Locate every malaria parasite.
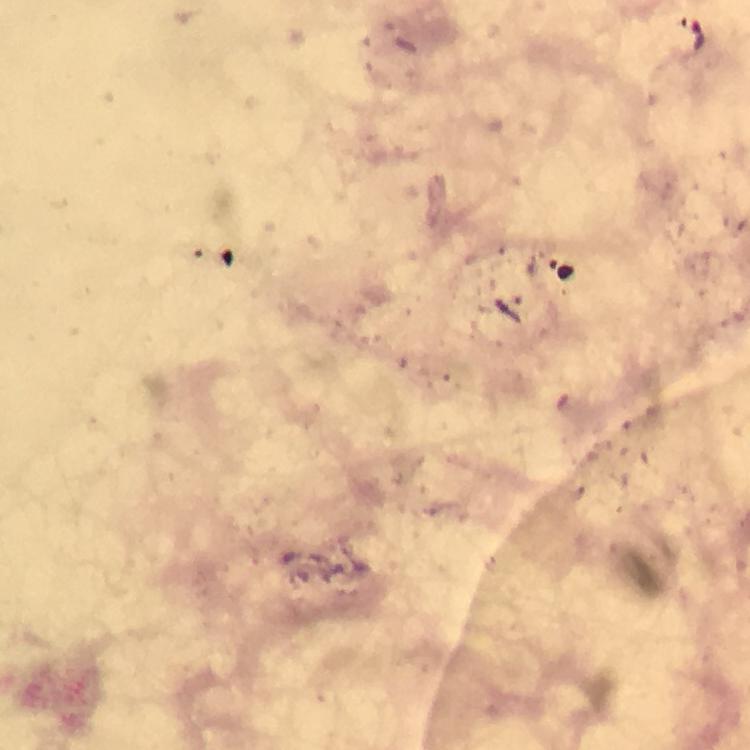

Approximate centers as [x, y] in pixels.
Malaria parasites: [697, 36].

preparation = thick smear
stain = Giemsa
immersion oil = used
magnification = 100x
image size = 750×750 pixels
cropped from = a single field of view
context = from a diagnostic examination for malaria
capture = smartphone mounted on the microscope